Report the malaria status of this cell.
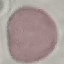

It is uninfected.

stain = Giemsa
preparation = thin blood smear
image type = automatically extracted cell patch, resized to 64 × 64 pixels
capture = smartphone through the microscope eyepiece